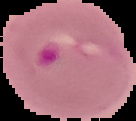
{
  "malaria_status": "parasitized",
  "image_type": "segmented cell region on a black background",
  "image_size": "136×121 pixels",
  "preparation": "thin blood film"
}